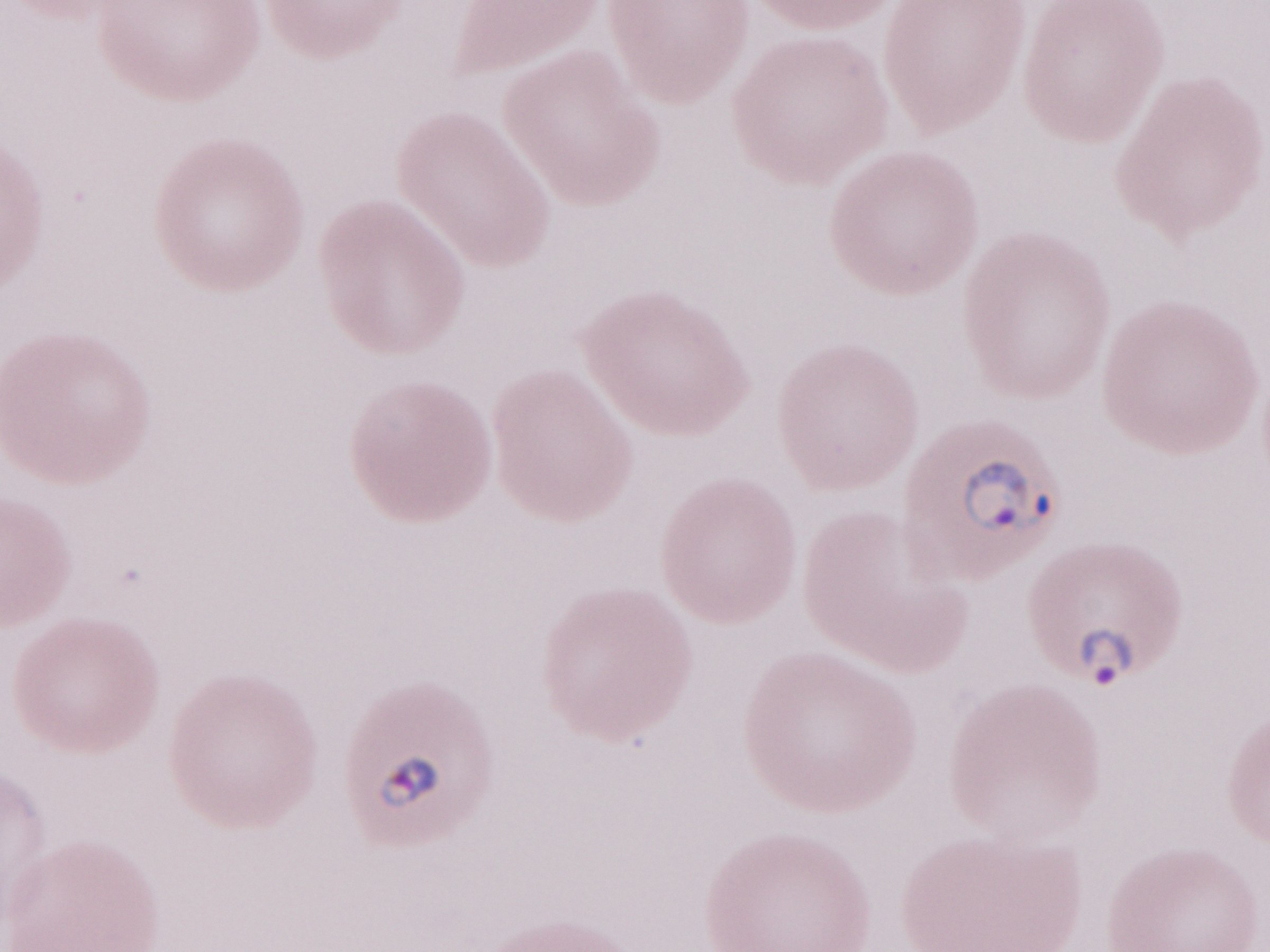
Malaria diagnosis (patient-level): positive. May-Grünwald-Giemsa (MGG) stain. Olympus BX43 microscope, Olympus DP73 camera. Thin peripheral-blood smear. Image is 1270×952 pixels. 1,000x magnification. Single field of view.